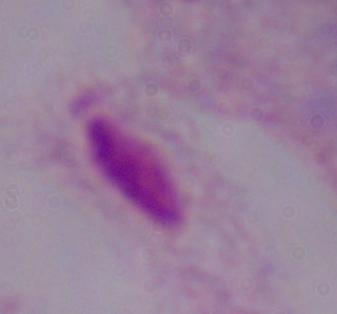

Photomicrograph. 1000x magnification. A trichomonad is shown.